Classify this cell by malaria status.
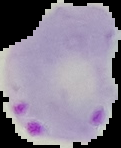

It is parasitized.

Image is 121×148 pixels. From a thin blood film. Segmented cell region on a black background.